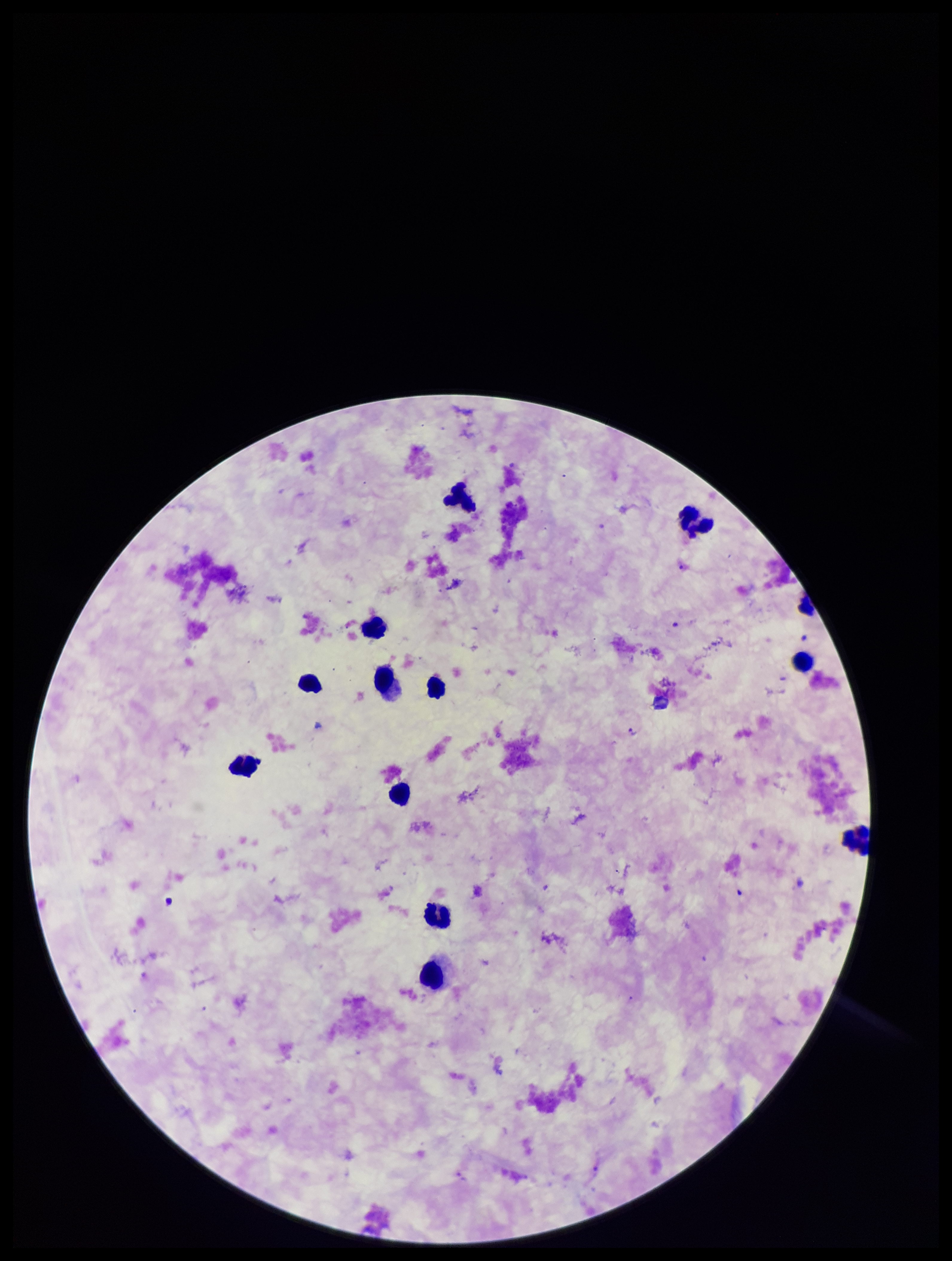
Summary:
  - Parasite count: 1
  - Image size: 952×1261 pixels
  - Capture: smartphone photograph through the microscope eyepiece
  - Leukocyte count: 13
  - Plasmodium parasites: detected
  - Preparation: thick
  - Field of view: one from this slide
  - Stain: Giemsa
  - Patient malaria status: infected
  - Species reported for this patient: Plasmodium falciparum